Identify the parasite.
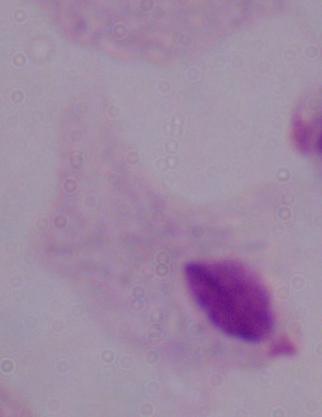
A trichomonad.

Summary:
  - Magnification: 1000x
  - Modality: micrograph